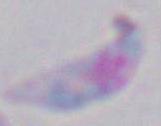 1000x magnification. Micrograph. Toxoplasma gondii is shown.